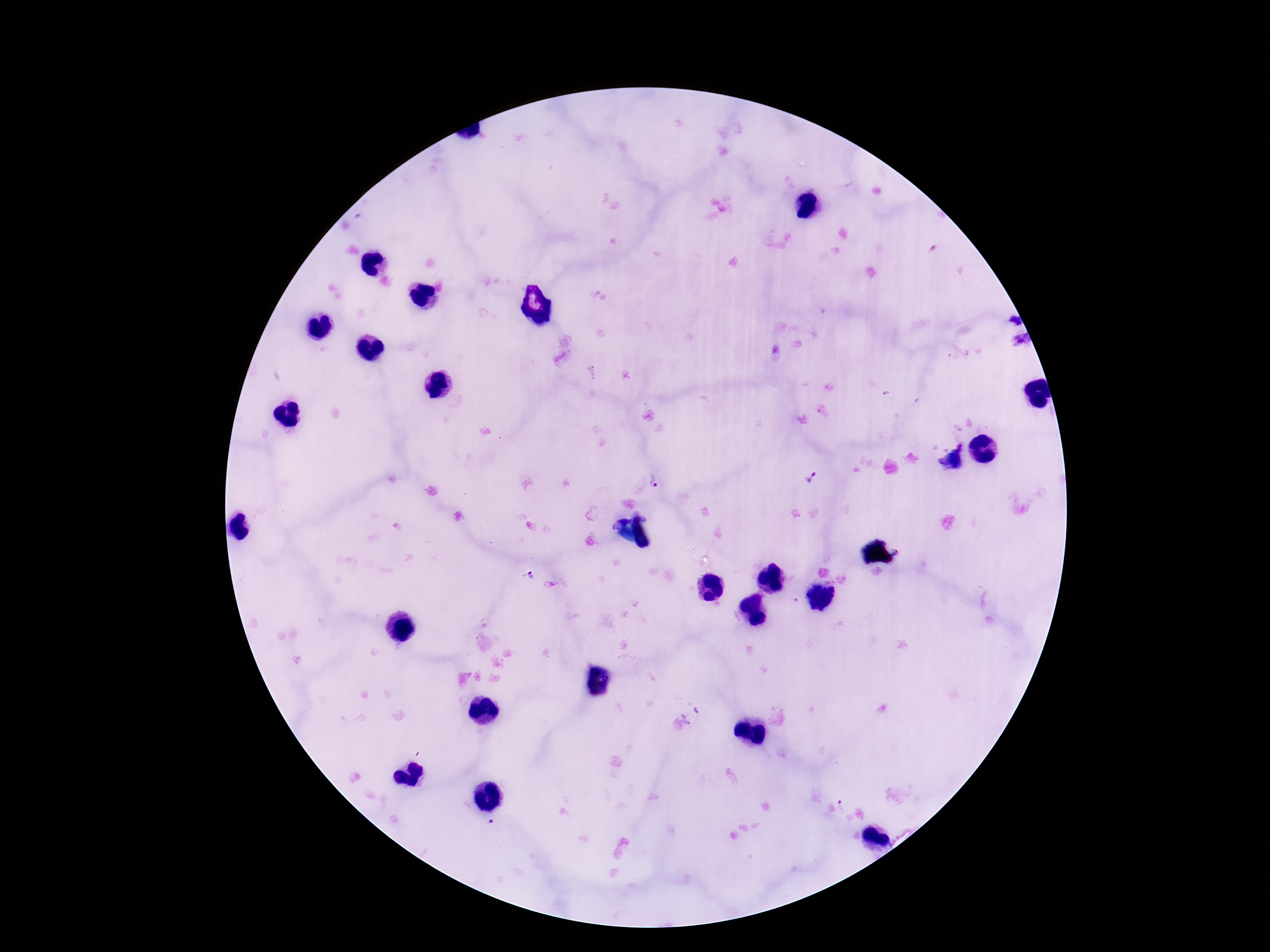

{
  "image_size": "1270×952 pixels",
  "plasmodium_parasite_locations": "approximate centers as {x, y} in pixels: {813, 477}, {655, 480}, {531, 576}",
  "field_of_view": "one from this slide",
  "patient_malaria_status": "positive",
  "stain": "Giemsa",
  "preparation": "thick peripheral-blood smear",
  "capture": "smartphone camera through the microscope eyepiece",
  "magnification": "100x"
}